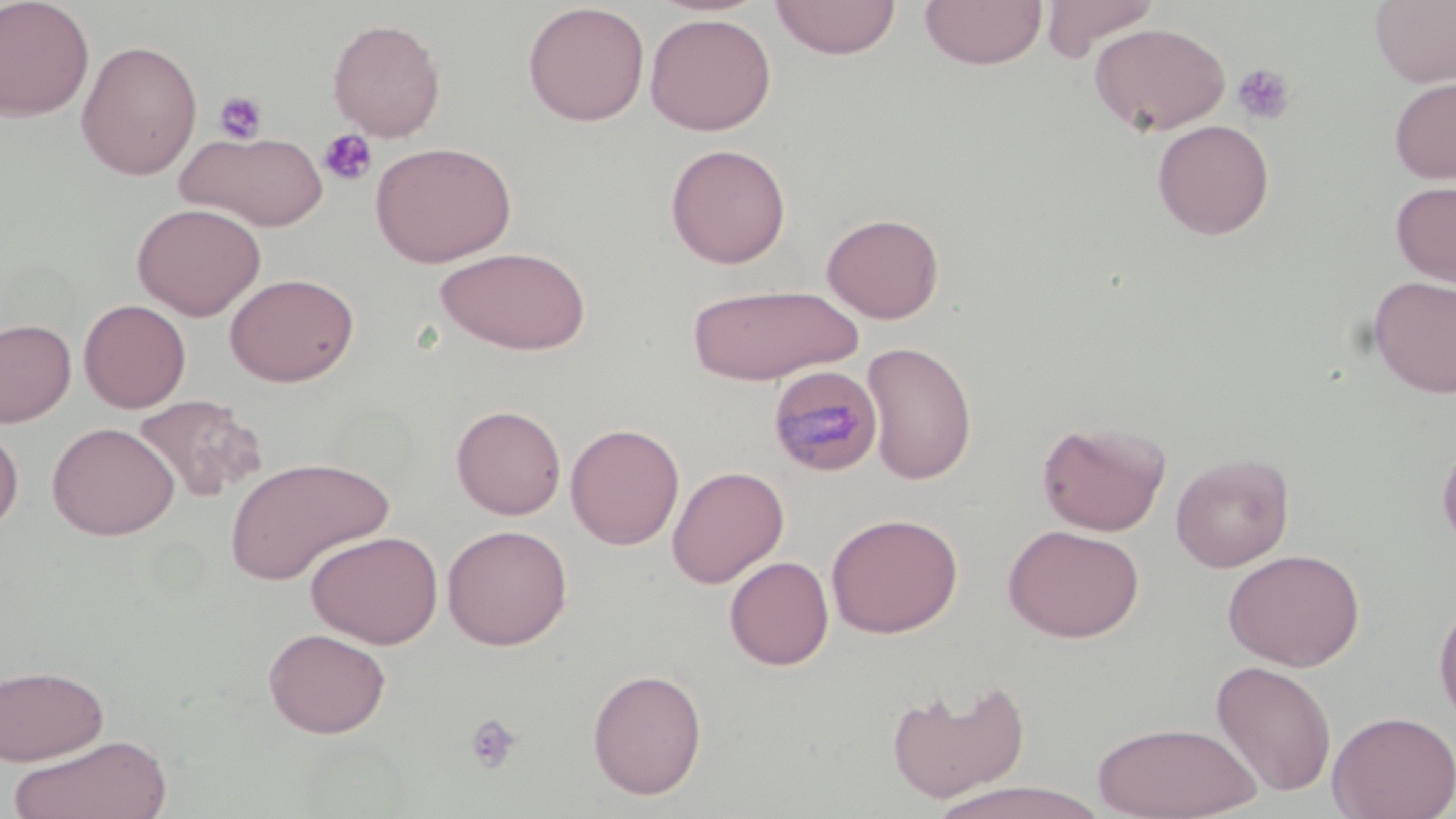

Summary:
  - Coordinate format: approximate bounding boxes as (x1,y1)-(x2,y2) corner pairs in pixels
  - Platelet locations: (1232,63)-(1295,125), (213,91)-(267,145), (318,128)-(377,187), (464,713)-(523,775)
  - Uninfected red blood cell locations: (0,0)-(95,121), (769,0)-(902,60), (920,0)-(1046,69), (1039,0)-(1161,61), (1371,0)-(1456,87), (522,2)-(650,126), (644,12)-(776,136), (327,18)-(446,141), (1090,22)-(1230,136), (76,39)-(203,180), (1389,77)-(1456,184), (1151,119)-(1275,240), (177,130)-(330,231), (370,141)-(516,267), (665,143)-(791,268), (1390,179)-(1456,288), (132,202)-(267,320), (821,212)-(945,323), (435,246)-(591,355), (224,272)-(359,387), (1369,275)-(1456,398), (687,283)-(863,384), (79,299)-(191,413), (0,317)-(77,427), (861,340)-(978,485), (132,394)-(267,503), (451,404)-(566,519), (1036,419)-(1170,536), (46,421)-(180,540), (0,423)-(24,536), (565,423)-(685,550), (1436,439)-(1456,552), (1170,453)-(1295,572), (224,455)-(394,585), (667,465)-(789,588), (826,512)-(963,639), (441,524)-(573,650), (1003,524)-(1145,643), (305,529)-(443,649), (1222,548)-(1365,671), (724,556)-(835,671), (1433,594)-(1456,730), (263,627)-(391,738), (1211,660)-(1337,797), (0,663)-(109,765), (587,668)-(707,799), (887,678)-(1031,803), (1327,710)-(1456,819), (1091,720)-(1262,818), (8,734)-(172,819), (929,781)-(1109,818)
  - Plasmodium malariae-infected red blood cell locations: (767,364)-(884,477)
  - Slide-level diagnosis: Plasmodium malariae
  - Field of view: single
  - Preparation: thin blood smear
  - Image size: 1456×819 pixels
  - Magnification: 1000x
  - Modality: optical microscopy
  - Stain: May-Grünwald-Giemsa